Assess this cell for malaria.
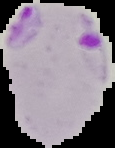

It is parasitized.

From a thin blood smear. Image is 115×148 pixels. Segmented cell region on a black background.